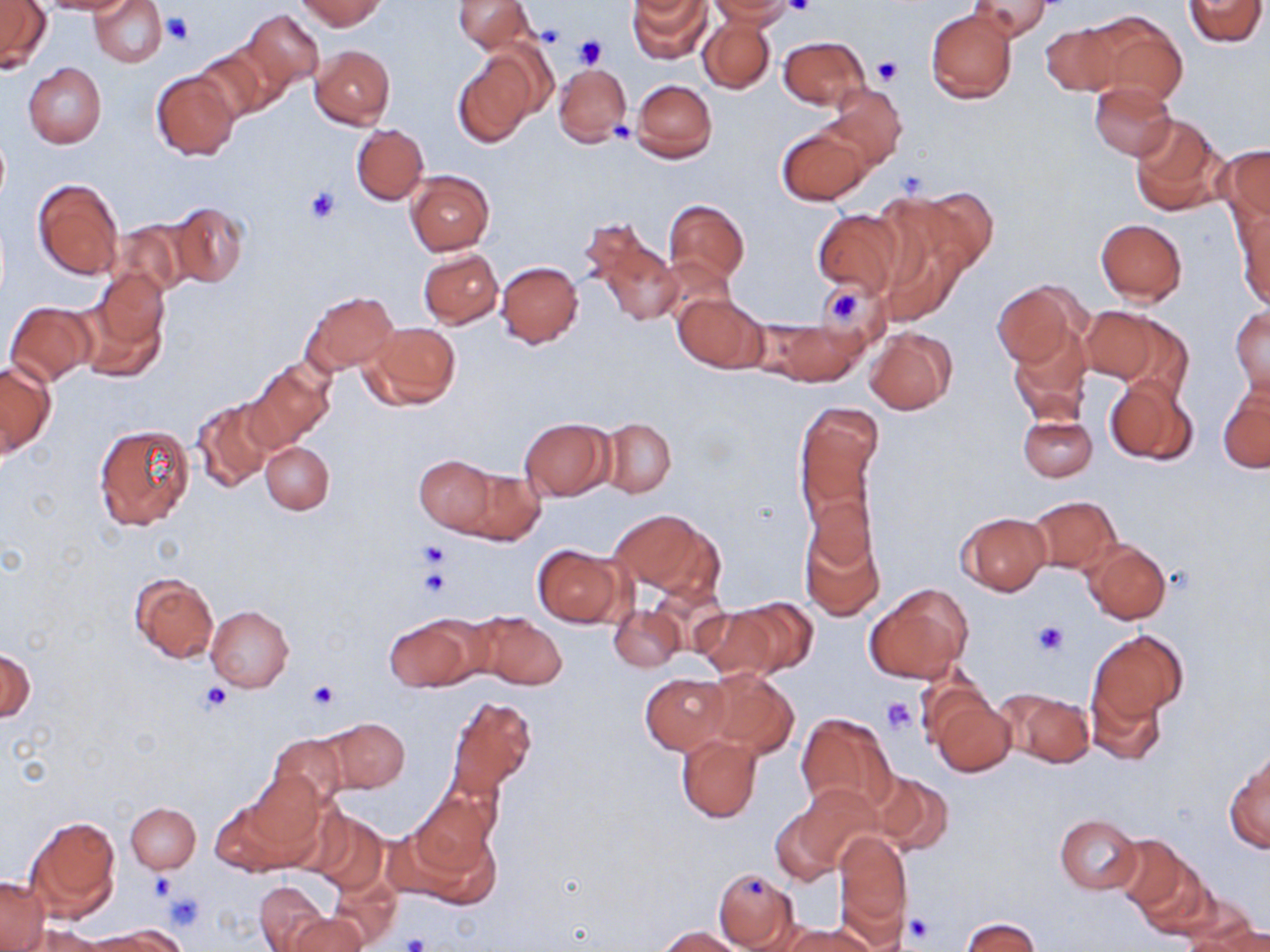 Approximate bounding boxes as [x1, y1, x2, y2] in pixels. Uninfected red blood cell locations: [38, 0, 131, 14], [90, 0, 167, 66], [296, 0, 385, 31], [454, 0, 535, 53], [628, 0, 710, 64], [706, 0, 797, 25], [968, 0, 1053, 43], [1182, 0, 1267, 47], [1, 2, 51, 74], [242, 9, 325, 92], [925, 9, 1018, 105], [1083, 10, 1187, 107], [699, 17, 776, 93], [1040, 23, 1122, 96], [779, 36, 871, 111], [189, 43, 279, 125], [309, 45, 395, 129], [452, 52, 537, 147], [24, 63, 106, 148], [553, 63, 632, 148], [151, 71, 240, 160], [631, 79, 717, 163], [1090, 83, 1176, 160], [822, 84, 908, 170], [1127, 112, 1228, 217], [352, 123, 428, 204], [777, 123, 872, 205], [1221, 145, 1269, 231], [405, 170, 494, 255], [31, 177, 125, 280], [885, 186, 996, 288], [663, 197, 749, 288], [163, 201, 249, 290], [812, 207, 905, 297], [1235, 208, 1270, 311], [1095, 218, 1188, 304], [109, 220, 193, 299], [586, 225, 685, 328], [418, 248, 503, 327], [496, 261, 583, 348], [991, 281, 1084, 371], [812, 283, 879, 336], [78, 285, 169, 382], [302, 289, 399, 374], [673, 292, 768, 373], [4, 301, 97, 386], [1230, 305, 1270, 396], [1079, 307, 1173, 389], [758, 317, 868, 385], [362, 322, 461, 410], [1009, 326, 1093, 424], [864, 328, 957, 415], [0, 360, 55, 458], [247, 360, 335, 451], [1104, 375, 1199, 468], [1218, 381, 1269, 473], [192, 397, 277, 491], [794, 404, 885, 532], [1018, 414, 1096, 482], [519, 417, 614, 500], [601, 417, 676, 498], [95, 423, 195, 529], [260, 441, 334, 514], [414, 454, 499, 534], [453, 465, 546, 545], [1026, 496, 1121, 575], [607, 507, 721, 603], [958, 512, 1050, 595], [799, 514, 885, 622], [1082, 540, 1171, 624], [532, 544, 624, 627], [131, 573, 218, 662], [864, 584, 974, 684], [696, 602, 802, 679], [609, 604, 683, 672], [206, 605, 293, 691], [471, 611, 566, 690], [383, 614, 482, 691], [1088, 629, 1188, 720], [1, 648, 34, 724], [705, 668, 799, 758], [915, 671, 994, 749], [640, 673, 730, 753], [1086, 685, 1166, 766], [996, 687, 1095, 768], [446, 696, 537, 797], [930, 696, 1016, 776], [796, 712, 898, 814], [322, 718, 410, 793], [267, 733, 348, 809], [675, 733, 762, 823], [1226, 751, 1269, 853], [871, 772, 953, 856], [246, 774, 330, 865], [792, 782, 882, 873], [419, 783, 500, 873], [210, 800, 294, 876], [125, 802, 200, 872], [304, 809, 389, 895], [394, 810, 502, 909], [771, 811, 841, 884], [1054, 814, 1143, 894], [26, 817, 120, 919], [832, 830, 912, 941], [1115, 833, 1190, 913], [1130, 856, 1221, 938], [712, 865, 800, 951], [327, 874, 401, 946], [0, 876, 47, 950], [254, 882, 328, 950], [1184, 901, 1267, 949], [289, 912, 365, 952], [961, 917, 1039, 951], [781, 924, 879, 952], [101, 925, 190, 951], [1190, 925, 1270, 951], [31, 926, 116, 952], [658, 926, 741, 951], [77, 931, 166, 951]. Platelet locations: [784, 0, 815, 17], [162, 12, 194, 46], [537, 23, 566, 47], [575, 36, 607, 69], [871, 56, 902, 85], [611, 121, 636, 143], [304, 187, 338, 225], [819, 282, 871, 332], [416, 540, 449, 569], [415, 566, 450, 599], [1032, 620, 1068, 657], [307, 680, 338, 710], [202, 681, 232, 712], [881, 697, 917, 734], [149, 873, 176, 900], [743, 875, 768, 901], [163, 891, 206, 931], [904, 915, 934, 944], [399, 932, 431, 952]. Slide-level diagnosis: negative for blood parasites. 1000x magnification. Image is 1270×952 pixels. One field of a larger specimen. May-Grünwald-Giemsa stain. Thin blood smear. Optical microscopy.